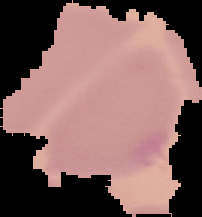

image_type: segmented cell region on a black background
preparation: thin blood film
image_size: 202×217 pixels
result: no Plasmodium parasites seen